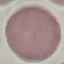
Summary:
  - Malaria status: uninfected
  - Stain: Giemsa
  - Preparation: thin blood smear
  - Capture: smartphone through the microscope eyepiece
  - Image type: cell patch, automatically extracted from a larger field of view and resized to 64 × 64 pixels